Classify this cell by malaria status.
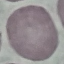

It is uninfected.

image type = cell patch, automatically extracted from a larger field of view and resized to 64 × 64 pixels
capture = smartphone through the microscope eyepiece
stain = Giemsa
preparation = thin blood film